Outline each Plasmodium vivax-infected red blood cell.
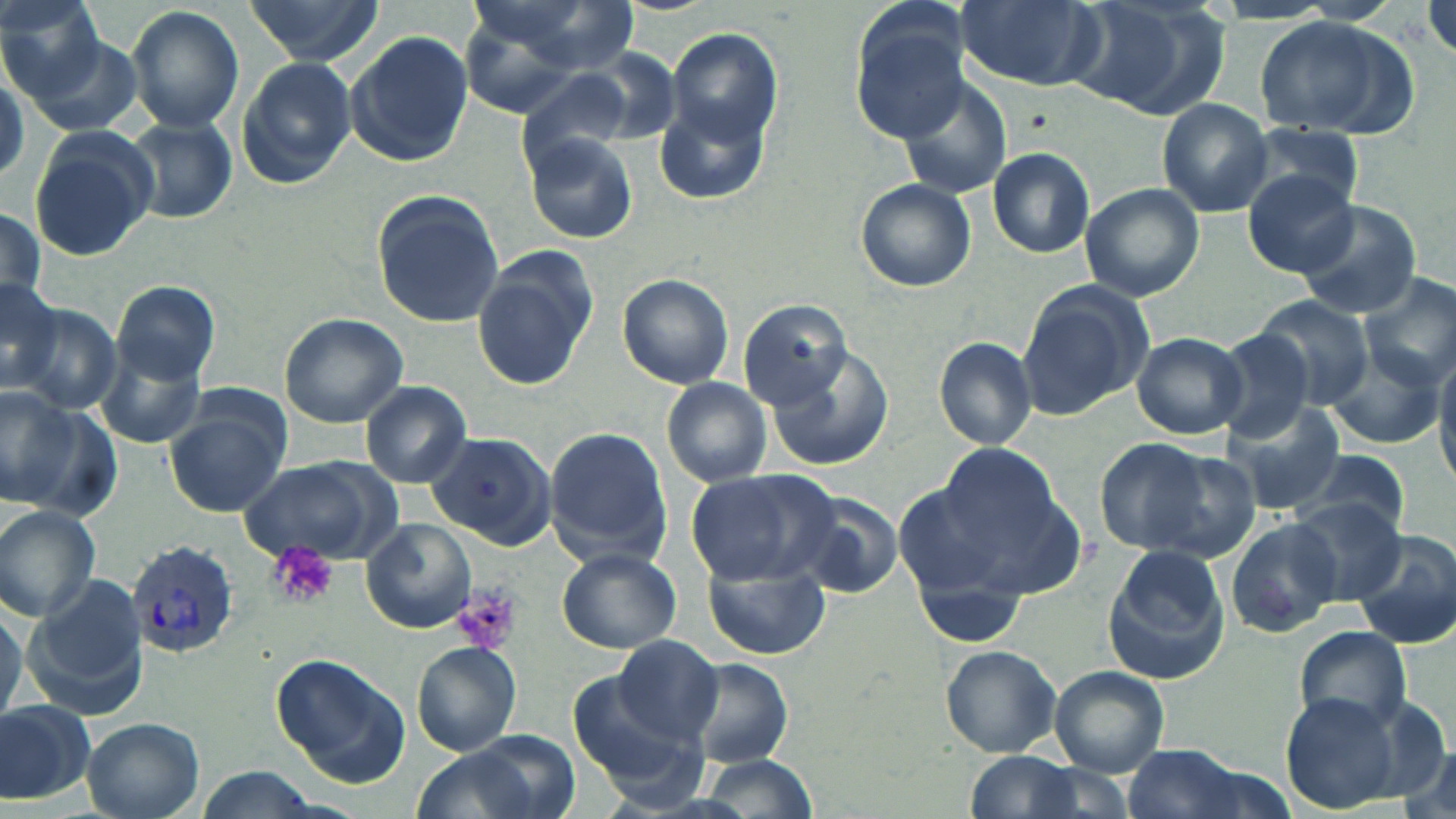
Approximate bounding boxes as (x1,y1)-(x2,y2) corner pairs in pixels.
Plasmodium vivax-infected red blood cells: (125,540)-(238,657).

{
  "slide_level_diagnosis": "Plasmodium vivax",
  "platelet_locations": "approximate bounding boxes as (x1,y1)-(x2,y2) corner pairs in pixels: (270,542)-(339,609), (453,585)-(521,656)",
  "modality": "light microscopy",
  "stain": "May-Grünwald-Giemsa",
  "preparation": "thin blood film",
  "image_size": "1456×819 pixels",
  "uninfected_red_blood_cell_locations": "approximate bounding boxes as (x1,y1)-(x2,y2) corner pairs in pixels: (243,0)-(379,66), (466,0)-(638,75), (848,0)-(971,143), (958,0)-(1104,90), (1066,0)-(1229,118), (1425,1)-(1456,63), (0,2)-(112,106), (128,5)-(244,135), (1251,14)-(1413,139), (666,29)-(782,141), (346,30)-(474,168), (23,34)-(144,140), (235,56)-(356,189), (517,73)-(636,175), (900,78)-(1015,199), (1158,99)-(1272,217), (655,102)-(768,205), (119,117)-(237,223), (1236,123)-(1366,219), (28,128)-(157,261), (523,131)-(637,243), (988,146)-(1096,257), (1244,172)-(1358,277), (856,179)-(976,292), (1078,182)-(1204,301), (371,191)-(505,327), (1292,200)-(1425,320), (0,205)-(45,309), (473,251)-(597,391), (618,273)-(734,388), (0,275)-(65,393), (1358,275)-(1456,391), (113,281)-(221,385), (1016,282)-(1153,420), (1252,295)-(1378,408), (739,300)-(859,417), (13,305)-(120,416), (279,313)-(408,428), (1208,327)-(1318,443), (1132,333)-(1248,438), (95,338)-(207,451), (935,338)-(1037,449), (769,346)-(893,475), (1320,347)-(1446,451), (1433,347)-(1456,484), (662,379)-(770,487), (361,381)-(473,488), (0,389)-(98,515), (1221,401)-(1345,513), (164,406)-(288,517), (544,426)-(671,566), (426,432)-(556,548), (1090,437)-(1214,552), (929,441)-(1072,571), (1135,447)-(1263,566), (1294,449)-(1413,537), (237,457)-(398,565), (684,467)-(840,588), (893,480)-(1016,605), (792,492)-(906,602), (1282,499)-(1406,604), (0,505)-(102,623), (1225,518)-(1344,637), (363,520)-(477,633), (1351,530)-(1455,647), (1101,542)-(1233,682), (556,545)-(681,653), (704,560)-(829,660), (26,573)-(148,720), (0,601)-(26,727), (1294,625)-(1414,731), (612,633)-(723,743), (411,642)-(521,757), (941,646)-(1063,757), (268,652)-(411,789), (688,659)-(792,768), (1049,666)-(1170,776), (567,672)-(702,795), (1278,692)-(1410,809), (0,698)-(93,804), (80,717)-(205,818), (408,743)-(550,819), (1121,743)-(1264,819), (962,751)-(1087,819), (698,755)-(815,816)",
  "magnification": "1000x",
  "field_of_view": "single"
}